Describe the morphology of the erythrocytes.
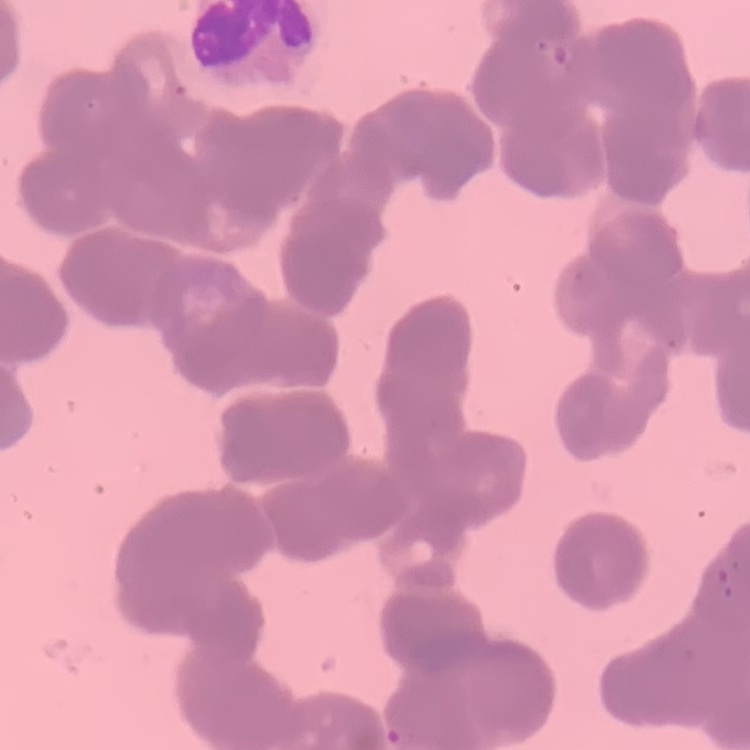
They show rouleaux formation.

Thin peripheral smear. Field's or Giemsa stain. Square crop of a larger photomicrograph.